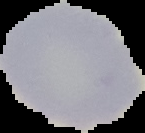

image_size: 145×133 pixels
image_type: cell region segmented out of the field of view; surrounding area masked to black
result: no malaria parasites detected
preparation: thin blood film